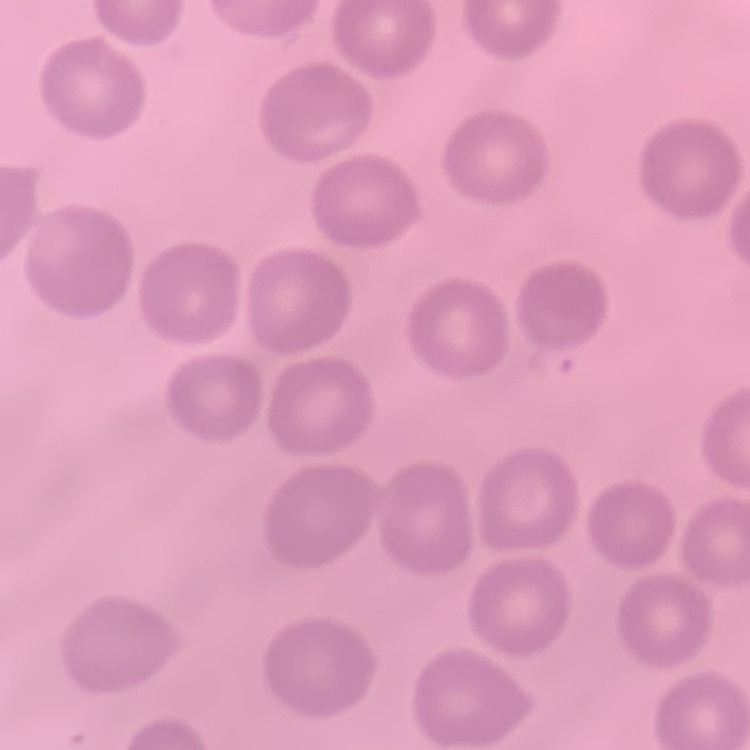
erythrocyte morphology = no rouleaux formation
image type = one tile cut from a larger photomicrograph
stain = Field's or Giemsa
preparation = thin peripheral smear